Assess this cell for malaria.
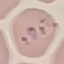

It is parasitized.

Giemsa-stained preparation. Thin blood smear. Photographed with a smartphone camera at the microscope eyepiece. Cell patch, automatically extracted from a larger field of view and resized to 64 × 64 pixels.